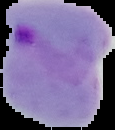

Image is 115×130 pixels. The area outside the segmented cell region is set to black. From a thin blood film. Result: Plasmodium parasites detected.